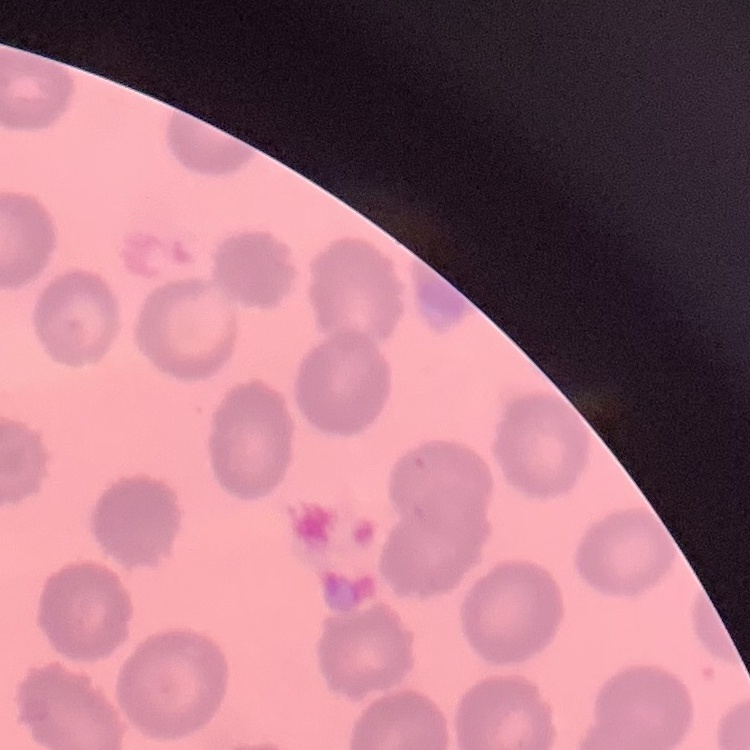

red_blood_cell_morphology: no rouleaux formation
preparation: thin peripheral smear
image_type: one tile cut from a larger photomicrograph
stain: Field's or Giemsa